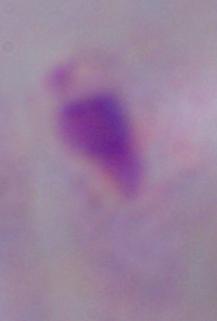

1000x magnification. A trichomonad is seen. Micrograph.